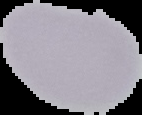
Summary:
  - Image type: segmented cell region with the area outside set to black
  - Preparation: thin blood smear
  - Image size: 142×115 pixels
  - Result: no Plasmodium parasites seen